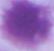

Summary:
  - Magnification: 1000x
  - Modality: photomicrograph
  - Identification: erythrocyte